Locate every P. falciparum parasite and give its life-cycle stage, and locate every leukocyte and any debris.
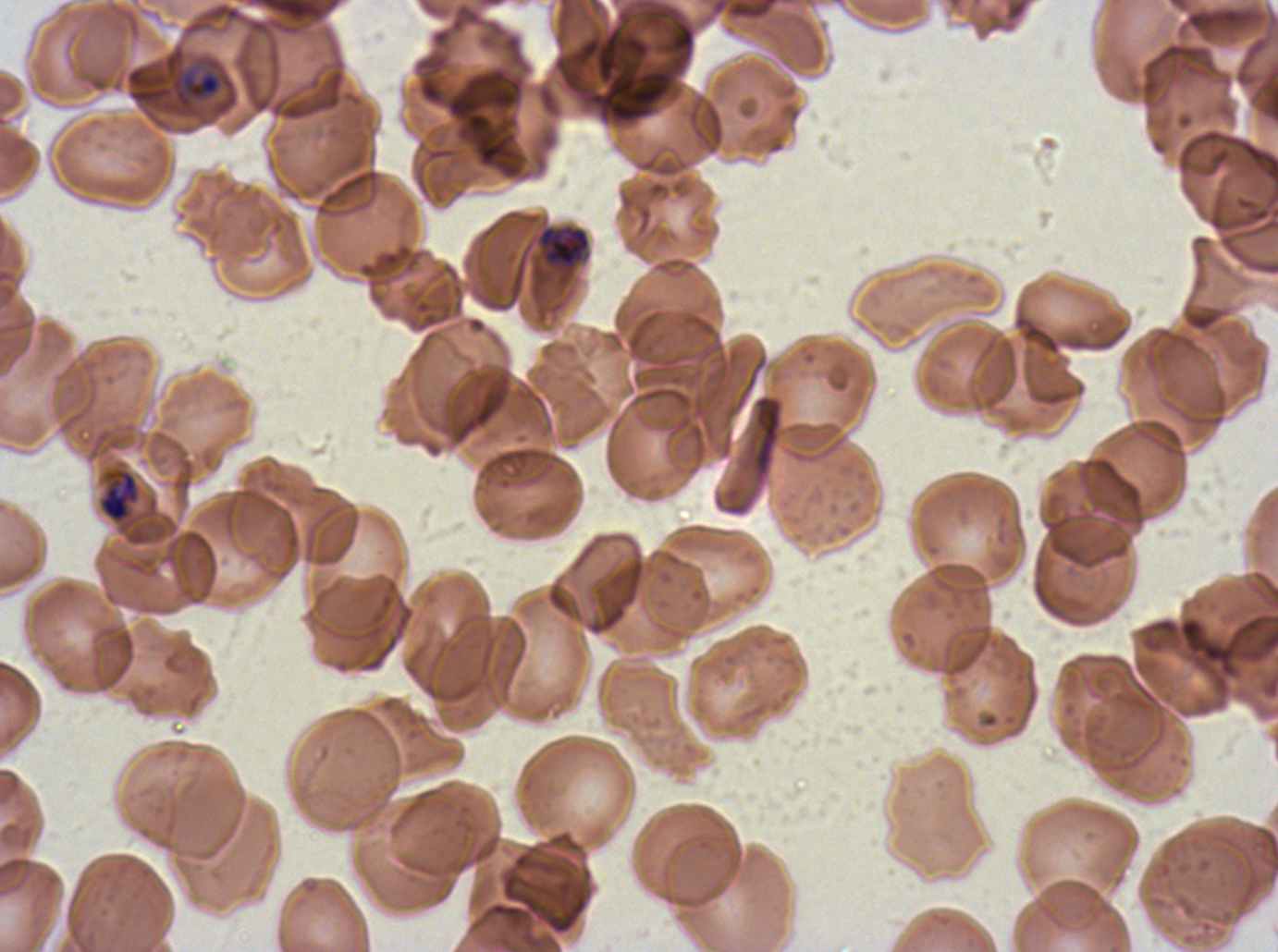
Approximate bounding rectangles given as corner coordinates in pixels from the top-left.
Late-ring/early-trophozoite forms: (x1=174, y1=70, x2=222, y2=110).
Late trophozoites: (x1=537, y1=224, x2=591, y2=270), (x1=98, y1=469, x2=140, y2=524).
No rings, mid trophozoites, early schizonts, late schizonts, segmenters, gametocytes, leukocytes, or debris observed.

specimen = P. falciparum from a patient in The Gambia, cultured ex vivo for 24 to 48 hours
image size = 1278×952 pixels
preparation = thin blood film
stain = Giemsa
field of view = sub-image separated from a larger composite
life-cycle stages observed = late-ring/early-trophozoite, late trophozoite